Locate every blood parasite and identify its species.
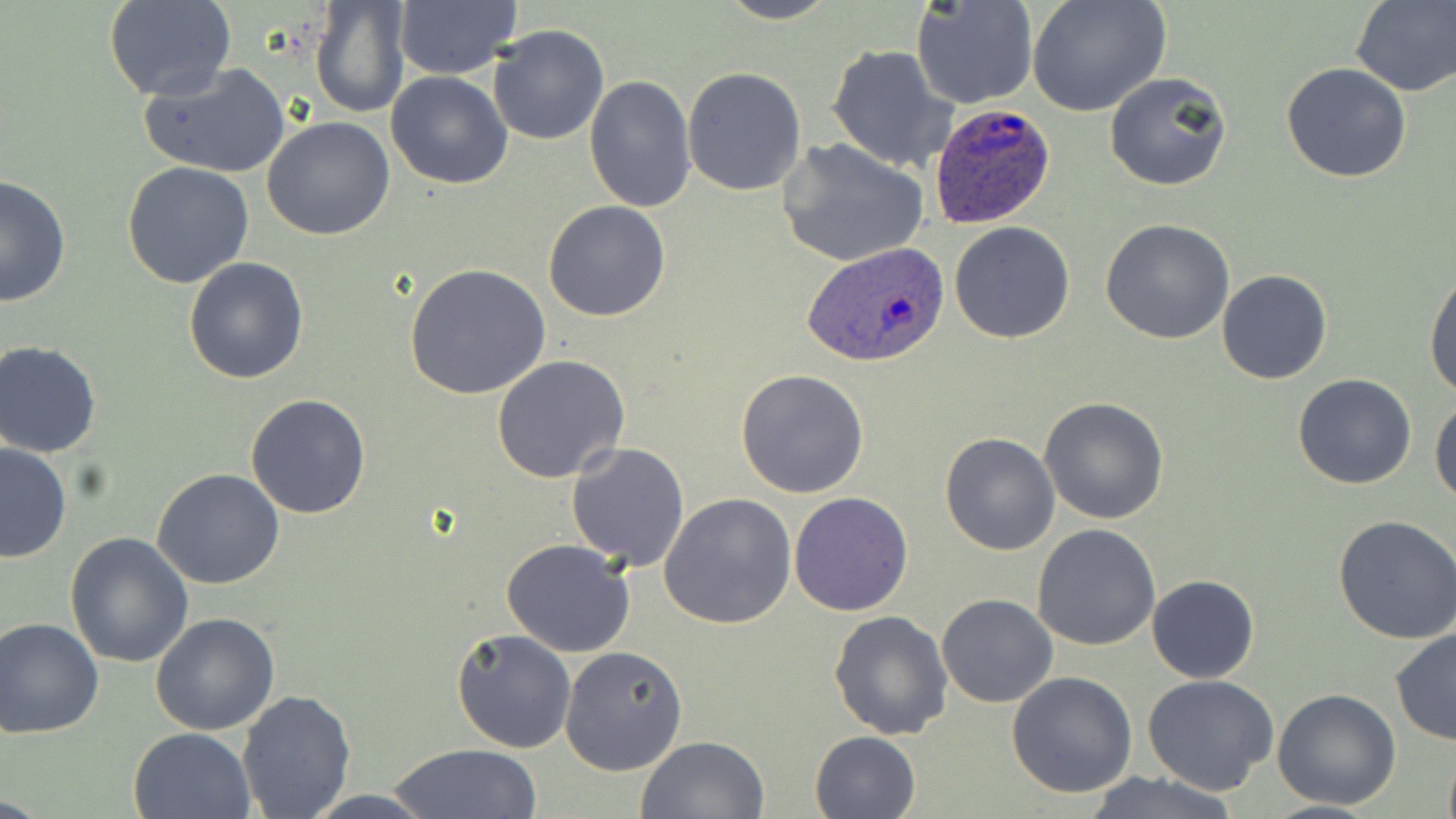
Approximate bounding boxes as named x1/y1/x2/y2 corners in pixels.
Plasmodium ovale-infected red blood cells: (x1=928, y1=103, x2=1057, y2=228), (x1=801, y1=240, x2=947, y2=368).
No Plasmodium falciparum, Plasmodium malariae, Plasmodium vivax, Babesia divergens, or Trypanosoma brucei observed.

Summary:
  - Uninfected red blood cell locations: (x1=103, y1=0, x2=237, y2=101), (x1=310, y1=0, x2=412, y2=120), (x1=713, y1=0, x2=842, y2=25), (x1=911, y1=0, x2=1039, y2=110), (x1=1027, y1=0, x2=1171, y2=118), (x1=1351, y1=0, x2=1456, y2=96), (x1=391, y1=2, x2=521, y2=80), (x1=487, y1=24, x2=609, y2=146), (x1=826, y1=45, x2=954, y2=175), (x1=1281, y1=62, x2=1413, y2=183), (x1=140, y1=63, x2=290, y2=179), (x1=681, y1=65, x2=807, y2=196), (x1=1103, y1=71, x2=1233, y2=192), (x1=385, y1=72, x2=512, y2=189), (x1=584, y1=74, x2=698, y2=215), (x1=263, y1=116, x2=397, y2=241), (x1=778, y1=138, x2=929, y2=268), (x1=122, y1=160, x2=255, y2=287), (x1=0, y1=175, x2=72, y2=307), (x1=543, y1=200, x2=671, y2=322), (x1=1100, y1=218, x2=1235, y2=344), (x1=949, y1=221, x2=1075, y2=343), (x1=184, y1=257, x2=310, y2=385), (x1=404, y1=262, x2=552, y2=400), (x1=1424, y1=267, x2=1456, y2=400), (x1=1217, y1=270, x2=1332, y2=386), (x1=1, y1=341, x2=103, y2=458), (x1=491, y1=354, x2=630, y2=483), (x1=736, y1=369, x2=870, y2=498), (x1=1293, y1=375, x2=1417, y2=490), (x1=245, y1=392, x2=373, y2=519), (x1=1429, y1=395, x2=1456, y2=507), (x1=1039, y1=397, x2=1169, y2=523), (x1=939, y1=431, x2=1061, y2=555), (x1=0, y1=442, x2=72, y2=563), (x1=565, y1=444, x2=691, y2=569), (x1=152, y1=468, x2=285, y2=589), (x1=788, y1=491, x2=913, y2=616), (x1=659, y1=492, x2=795, y2=630), (x1=1333, y1=516, x2=1456, y2=643), (x1=1032, y1=523, x2=1161, y2=651), (x1=66, y1=530, x2=195, y2=668), (x1=502, y1=539, x2=636, y2=658), (x1=1147, y1=573, x2=1259, y2=684), (x1=937, y1=593, x2=1057, y2=708), (x1=828, y1=609, x2=954, y2=740), (x1=149, y1=613, x2=279, y2=735), (x1=0, y1=616, x2=103, y2=739), (x1=451, y1=628, x2=578, y2=754), (x1=1389, y1=628, x2=1456, y2=745), (x1=560, y1=646, x2=689, y2=776), (x1=1006, y1=671, x2=1138, y2=797), (x1=1141, y1=673, x2=1280, y2=794), (x1=236, y1=689, x2=357, y2=818), (x1=1272, y1=689, x2=1402, y2=810), (x1=128, y1=726, x2=256, y2=819), (x1=809, y1=730, x2=921, y2=819), (x1=635, y1=735, x2=769, y2=818), (x1=390, y1=743, x2=544, y2=819), (x1=1441, y1=749, x2=1456, y2=819), (x1=1080, y1=771, x2=1241, y2=818), (x1=299, y1=791, x2=441, y2=819)
  - Slide-level diagnosis: Plasmodium ovale
  - Modality: optical microscopy
  - Preparation: thin blood smear
  - Field of view: single
  - Image size: 1456×819 pixels
  - Stain: May-Grünwald-Giemsa
  - Magnification: 1000x